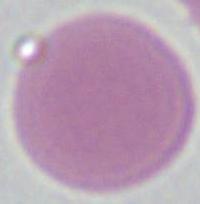
Photomicrograph. A red blood cell is shown. 1000x magnification.